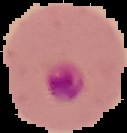

Summary:
  - Image type: cell region segmented out of the field of view; surrounding area masked to black
  - Result: Plasmodium parasites identified
  - Image size: 127×133 pixels
  - Preparation: thin blood smear